Classify this cell by malaria status.
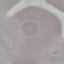
Uninfected.

{
  "preparation": "thin smear",
  "stain": "Giemsa",
  "image_type": "cell patch, automatically extracted from a larger field of view and resized to 64 × 64 pixels",
  "capture": "smartphone camera at the microscope eyepiece"
}